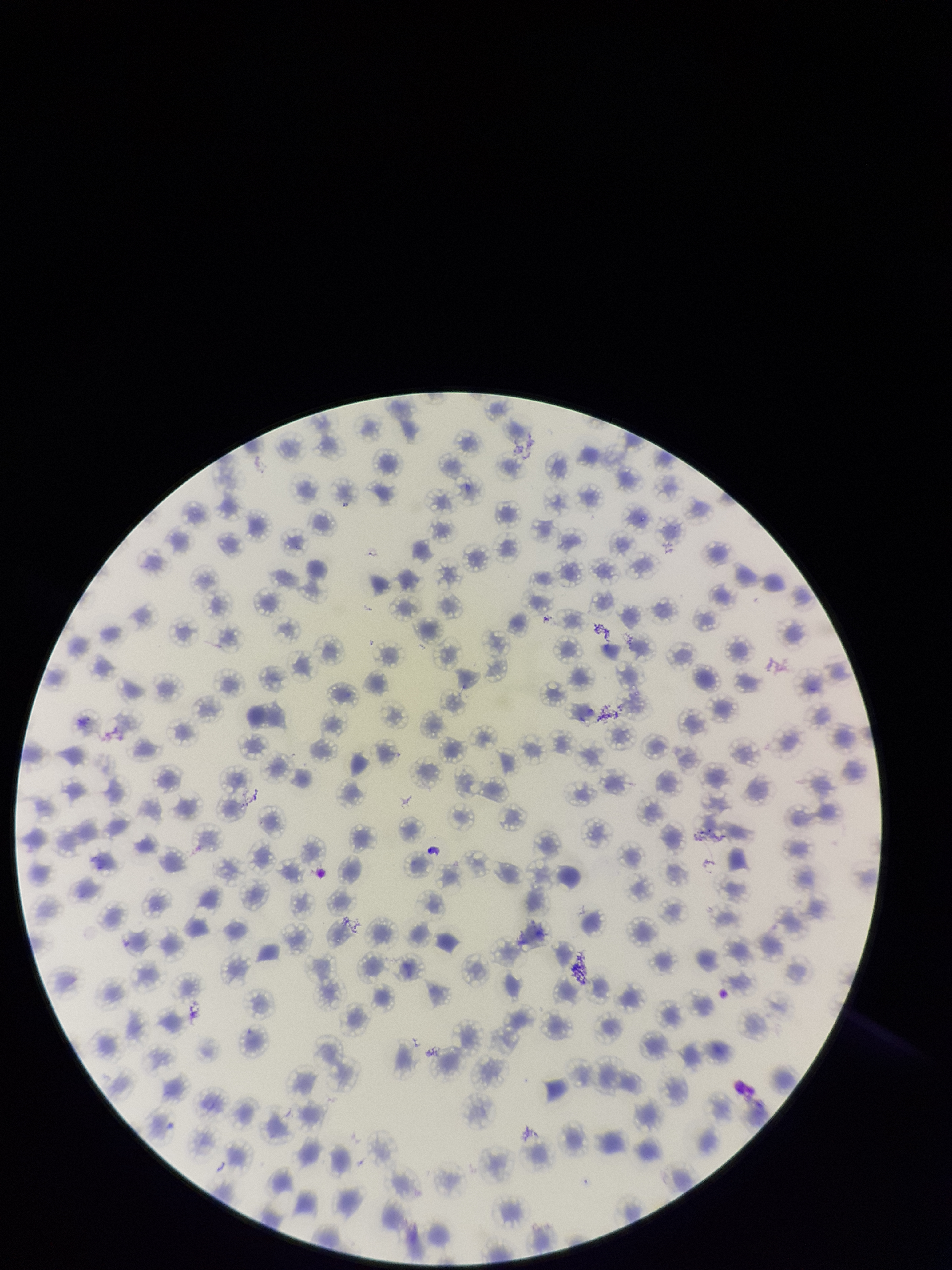

patient malaria status = infected
capture = smartphone photograph through the microscope eyepiece
image size = 952×1270 pixels
red blood cell count = 117
parasitized red blood cell count = 0
field of view = one from this slide
parasitized red blood cells = none detected
species reported for this patient = Plasmodium falciparum
preparation = thin
stain = Giemsa